Report the malaria status of this cell.
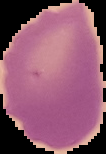

It is uninfected.

preparation = thin blood smear
image type = segmented cell region with the area outside set to black
image size = 106×154 pixels